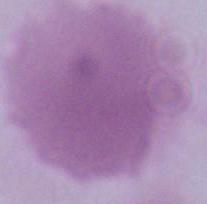

Summary:
  - Modality: photomicrograph
  - Magnification: 1000x
  - Identification: erythrocyte